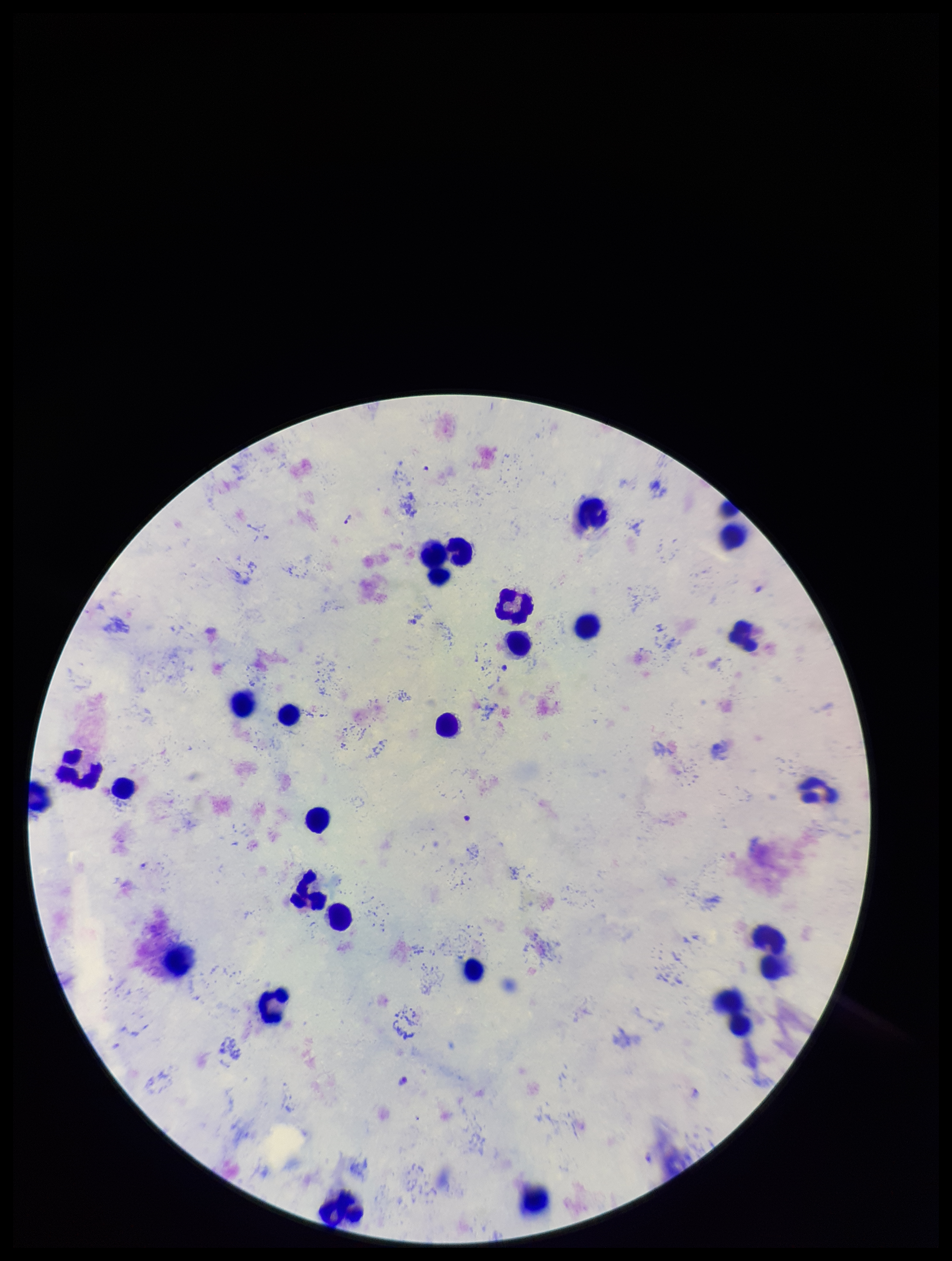

Summary:
  - Parasite count: 0
  - Capture: smartphone photograph through the microscope eyepiece
  - Field of view: one from this slide
  - Plasmodium parasites: none seen
  - Image size: 952×1261 pixels
  - Preparation: thick blood smear
  - Species reported for this patient: Plasmodium falciparum
  - Stain: Giemsa
  - Patient malaria status: infected
  - Leukocyte count: 25